Point out each malaria parasite.
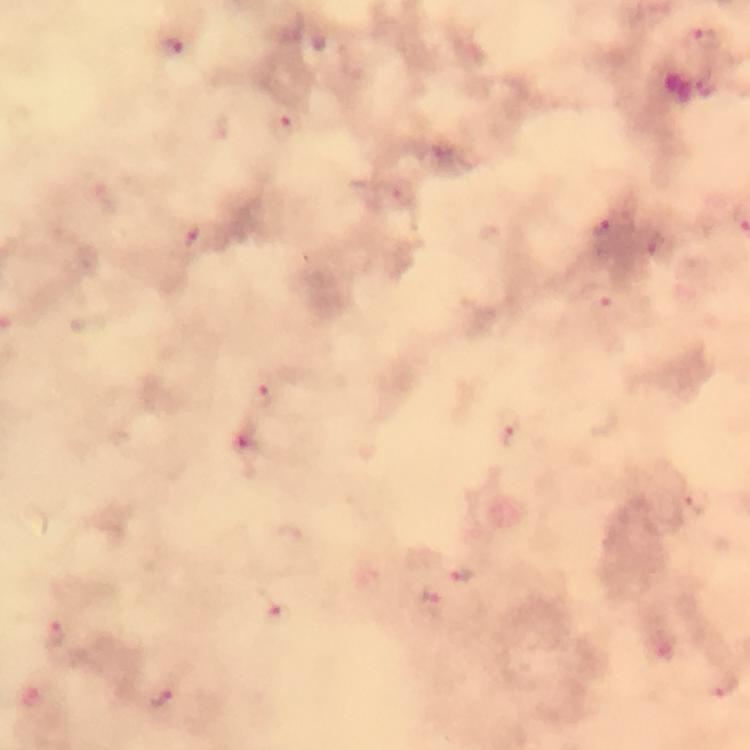

Approximate centers as (x, y) in pixels.
Malaria parasites: (704, 40), (170, 46), (709, 85), (284, 129), (607, 231), (192, 240), (656, 246), (600, 301), (265, 395), (512, 433), (246, 447), (465, 575), (431, 605), (279, 615), (53, 635), (721, 685), (161, 698).

Summary:
  - Cropped from: one field of view
  - Context: from a malaria diagnostic workup
  - Magnification: 100x
  - Image size: 750×750 pixels
  - Preparation: thick smear
  - Immersion oil: used
  - Capture: smartphone camera through the microscope
  - Stain: Giemsa